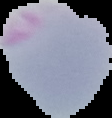
From a thin blood smear. Image is 112×118 pixels. Malaria status: parasitized. Cell region segmented out of the field of view; the surrounding area is masked to black.